Assess this cell for malaria.
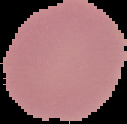
It is uninfected.

Summary:
  - Image size: 127×124 pixels
  - Preparation: thin blood film
  - Image type: segmented cell region on a black background